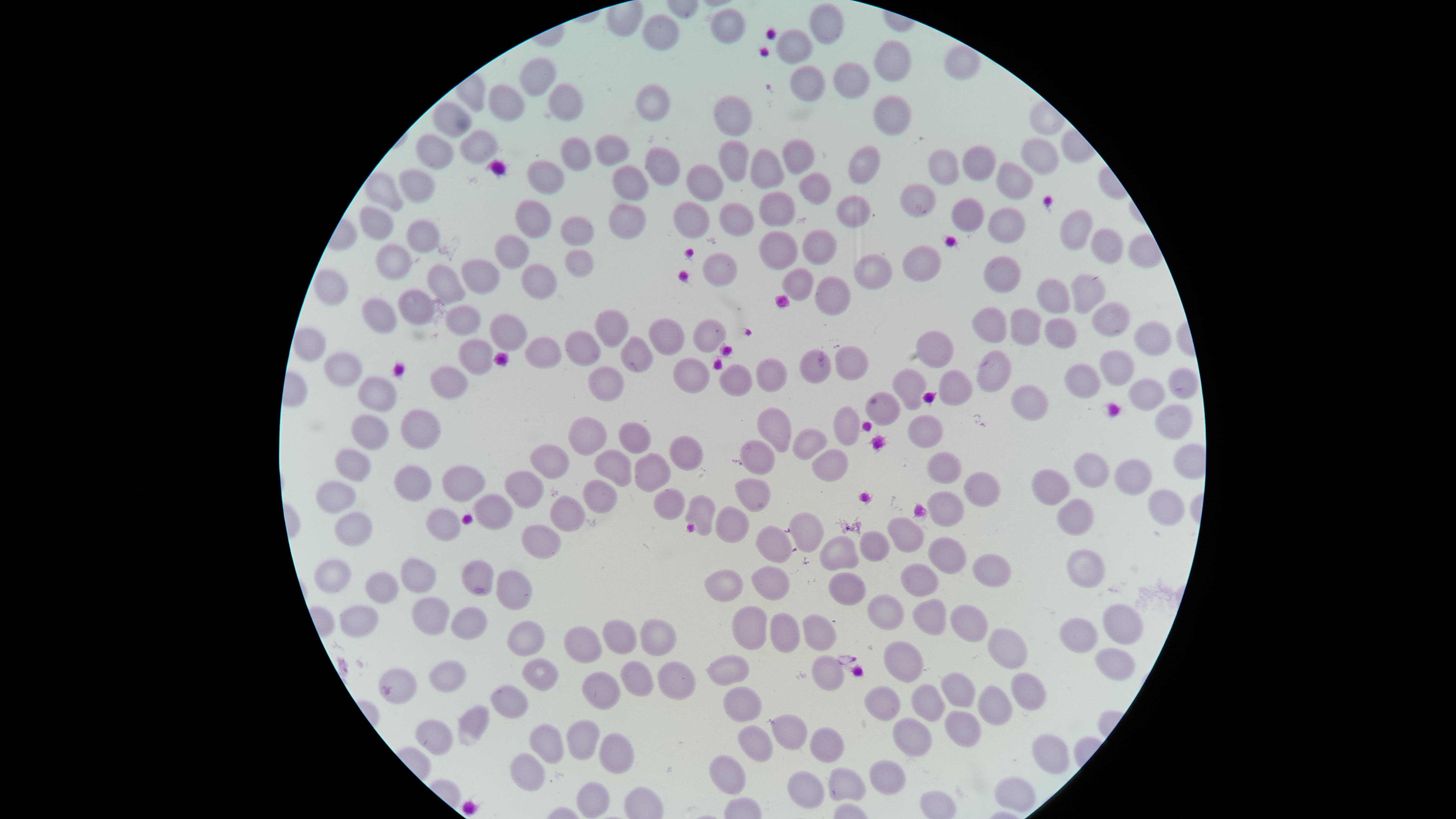
Approximate marker points as {x, y} in pixels.
Summary:
  - Uninfected RBCs: {721, 21}, {827, 26}, {663, 29}, {799, 46}, {892, 49}, {962, 61}, {539, 69}, {853, 80}, {807, 81}, {651, 98}, {505, 101}, {561, 101}, {730, 113}, {887, 116}, {452, 117}, {476, 146}, {608, 146}, {1044, 151}, {433, 153}, {800, 155}, {574, 156}, {730, 161}, {859, 163}, {976, 163}, {944, 164}, {661, 165}, {763, 170}, {544, 172}, {418, 179}, {704, 179}, {630, 181}, {1010, 181}, {382, 187}, {815, 189}, {918, 191}, {771, 208}, {843, 210}, {967, 212}, {533, 217}, {628, 219}, {375, 220}, {734, 220}, {1006, 220}, {693, 222}, {1076, 223}, {420, 233}, {578, 233}, {814, 242}, {776, 249}, {1099, 250}, {512, 251}, {390, 260}, {578, 260}, {925, 261}, {867, 265}, {479, 273}, {1007, 273}, {719, 274}, {449, 276}, {539, 277}, {799, 281}, {332, 284}, {1086, 286}, {828, 293}, {1052, 293}, {410, 306}, {378, 308}, {1118, 315}, {457, 317}, {610, 320}, {986, 323}, {1022, 327}, {1060, 329}, {507, 331}, {703, 331}, {667, 334}, {1145, 340}, {940, 341}, {306, 348}, {472, 348}, {578, 349}, {632, 353}, {538, 354}, {849, 359}, {346, 364}, {812, 364}, {696, 366}, {1111, 369}, {1001, 370}, {762, 372}, {447, 380}, {608, 381}, {737, 382}, {1083, 382}, {1181, 383}, {955, 384}, {381, 388}, {912, 391}, {1149, 395}, {1037, 399}, {884, 406}, {1168, 417}, {848, 422}, {770, 424}, {419, 427}, {924, 427}, {365, 428}, {629, 430}, {581, 434}, {814, 443}, {757, 450}, {685, 454}, {347, 457}, {614, 458}, {551, 461}, {829, 462}, {944, 464}, {650, 469}, {1082, 469}, {1133, 474}, {412, 479}, {980, 479}, {456, 480}, {1052, 483}, {522, 484}, {754, 493}, {332, 497}, {592, 499}, {669, 499}, {1165, 503}, {700, 508}, {493, 510}, {947, 510}, {569, 512}, {1076, 513}, {446, 522}, {731, 525}, {807, 528}, {906, 528}, {355, 529}, {541, 532}, {773, 539}, {877, 542}, {837, 554}, {946, 557}, {418, 572}, {986, 572}, {1084, 573}, {474, 574}, {334, 576}, {919, 580}, {762, 582}, {387, 583}, {723, 585}, {849, 585}, {505, 593}, {886, 607}, {928, 615}, {357, 619}, {427, 619}, {969, 622}, {467, 623}, {1119, 623}, {816, 627}, {751, 628}, {780, 628}, {617, 629}, {653, 632}, {1081, 635}, {523, 640}, {585, 641}, {1004, 648}, {903, 660}, {732, 663}, {1110, 665}, {828, 669}, {529, 677}, {669, 677}, {450, 678}, {633, 680}, {1028, 687}, {959, 688}, {399, 690}, {601, 695}, {507, 698}, {738, 698}, {928, 699}, {883, 700}, {988, 705}, {469, 716}, {965, 721}, {788, 728}, {436, 731}, {578, 733}, {906, 737}, {544, 744}, {819, 745}, {611, 747}, {757, 747}, {1048, 751}, {530, 765}, {727, 771}, {883, 772}, {841, 780}, {803, 783}, {589, 784}, {1017, 786}
  - Visible region: circular
  - Image size: 1456×819 pixels
  - Preparation: thin smear of blood
  - Field of view: single
  - Capture: smartphone photograph through the microscope eyepiece
  - Presence: no malaria parasites identified
  - Stain: Giemsa